Locate every Plasmodium falciparum-infected red blood cell.
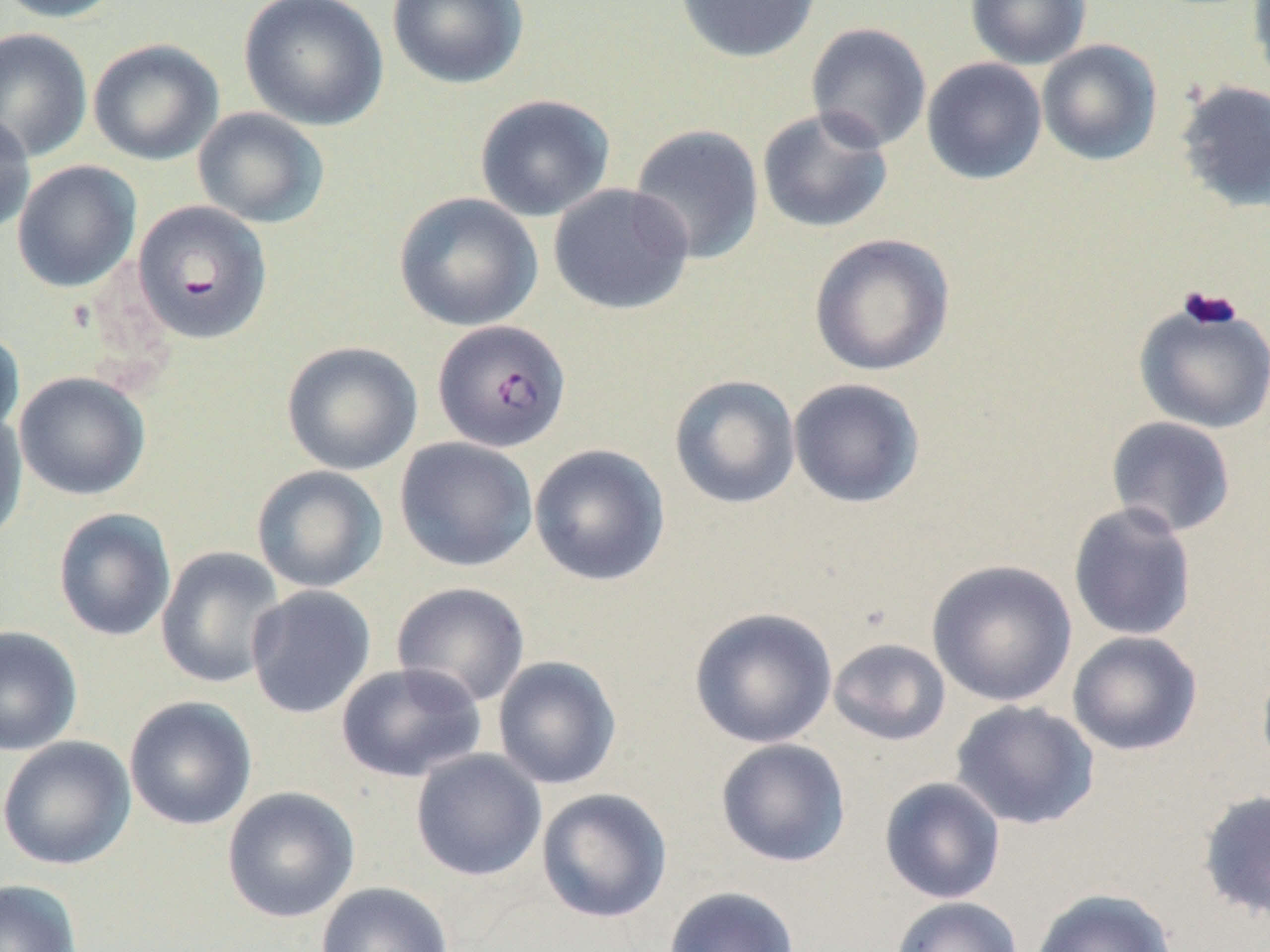

Approximate bounding boxes as [x1, y1, x2, y2] in pixels.
Plasmodium falciparum-infected red blood cells: [132, 201, 272, 345], [432, 319, 571, 453].

{
  "slide_level_diagnosis": "Plasmodium falciparum",
  "preparation": "thin blood film",
  "image_size": "1270×952 pixels",
  "modality": "light microscopy",
  "stain": "May-Grünwald-Giemsa",
  "magnification": "1000x",
  "uninfected_red_blood_cell_locations": "approximate bounding boxes as [x1, y1, x2, y2] in pixels: [0, 0, 126, 24], [239, 0, 389, 131], [386, 0, 530, 90], [674, 0, 821, 64], [965, 0, 1092, 69], [1248, 0, 1270, 95], [805, 22, 932, 152], [0, 27, 93, 162], [88, 39, 223, 165], [1036, 39, 1162, 166], [921, 57, 1047, 186], [1175, 80, 1270, 213], [473, 94, 616, 222], [192, 107, 330, 229], [757, 107, 894, 234], [0, 112, 36, 236], [629, 124, 765, 265], [12, 160, 141, 293], [548, 183, 695, 315], [393, 192, 543, 332], [808, 233, 955, 377], [1133, 300, 1270, 435], [0, 328, 25, 444], [281, 341, 423, 476], [14, 371, 151, 501], [669, 374, 801, 509], [788, 378, 926, 508], [0, 410, 28, 547], [1105, 416, 1237, 538], [394, 436, 538, 572], [529, 443, 671, 586], [251, 465, 388, 594], [1068, 502, 1198, 642], [53, 508, 176, 642], [155, 546, 287, 689], [927, 559, 1077, 707], [390, 581, 531, 708], [245, 584, 377, 720], [688, 606, 838, 749], [0, 625, 84, 757], [1067, 631, 1203, 756], [828, 638, 952, 746], [492, 655, 622, 790], [334, 662, 487, 783], [124, 696, 258, 831], [950, 700, 1100, 830], [0, 735, 136, 870], [715, 738, 851, 868], [410, 749, 547, 881], [879, 777, 1007, 904], [221, 786, 360, 923], [536, 787, 673, 924], [1197, 788, 1270, 923], [0, 878, 83, 952], [316, 881, 454, 952], [663, 885, 800, 952], [1030, 888, 1178, 952], [890, 896, 1023, 952]",
  "field_of_view": "single"
}